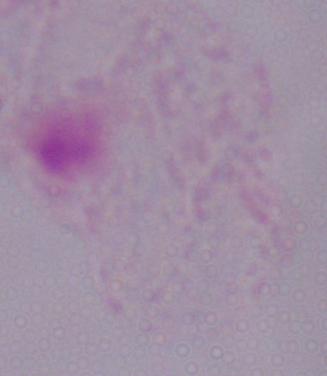
magnification = 1000x
modality = micrograph
identification = trichomonad